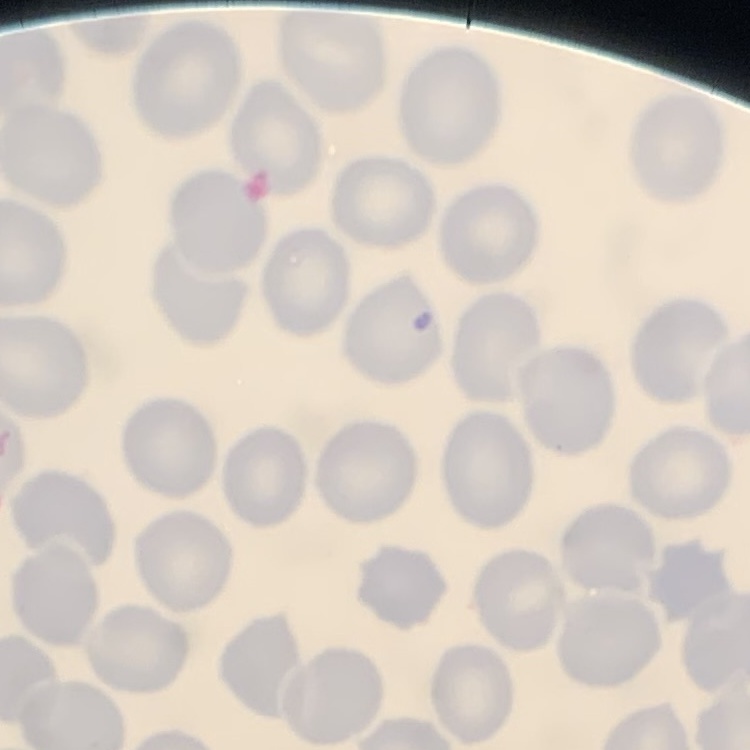

The erythrocytes exhibit no rouleaux formation. Thin peripheral smear. One tile cut from a larger photomicrograph. Field's or Giemsa stain.